Locate every blood parasite and identify its species.
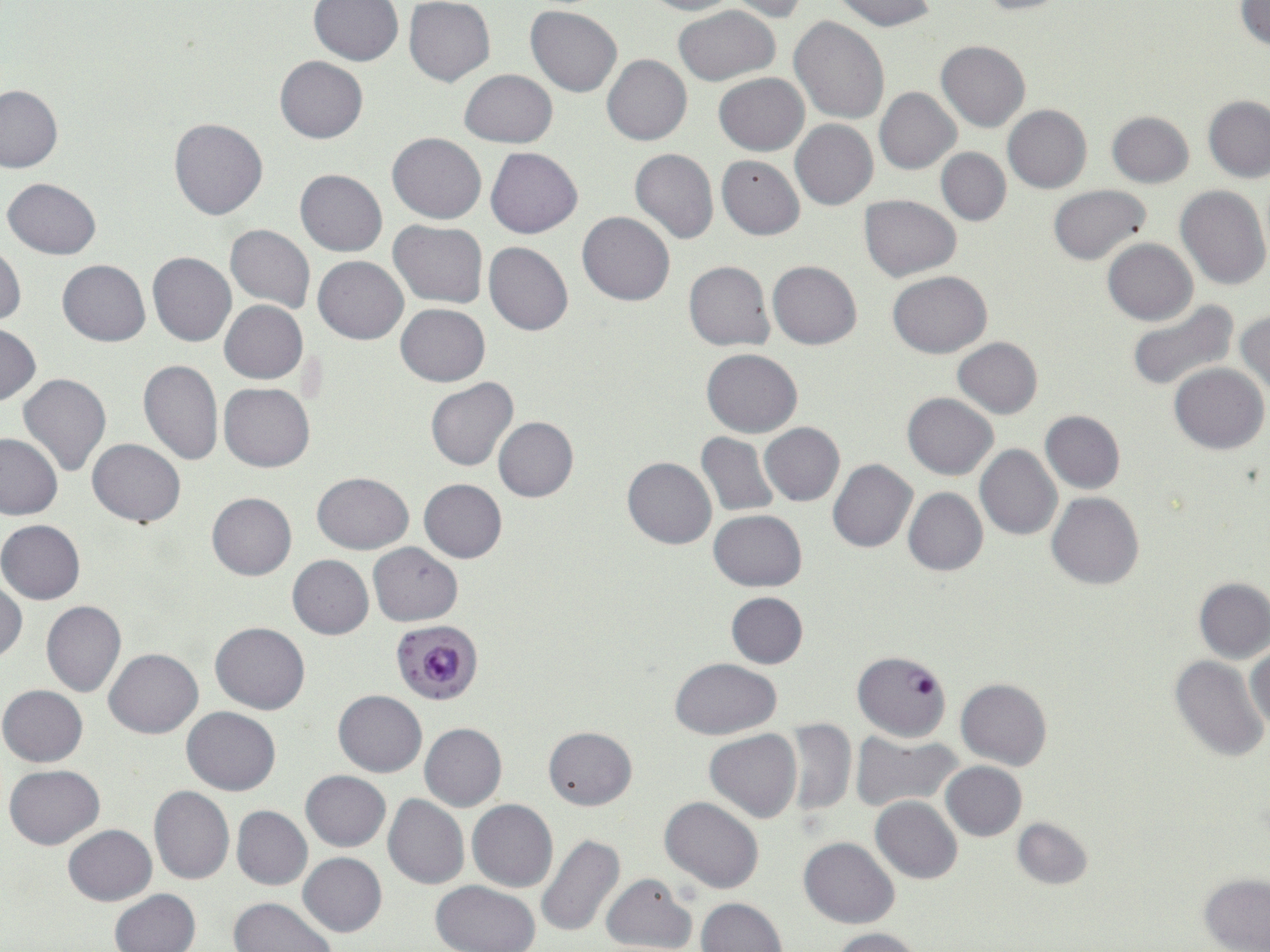

Approximate bounding boxes as named x1/y1/x2/y2 corners in pixels.
Plasmodium falciparum-infected red blood cells: (x1=390, y1=620, x2=482, y2=705), (x1=852, y1=650, x2=952, y2=741).
No Plasmodium ovale, Plasmodium malariae, Plasmodium vivax, Babesia divergens, or Trypanosoma brucei observed.

Uninfected red blood cell locations: (x1=640, y1=0, x2=741, y2=15), (x1=833, y1=0, x2=937, y2=30), (x1=969, y1=0, x2=1067, y2=15), (x1=310, y1=1, x2=403, y2=67), (x1=405, y1=1, x2=495, y2=86), (x1=724, y1=1, x2=809, y2=21), (x1=1235, y1=1, x2=1270, y2=51), (x1=673, y1=4, x2=780, y2=85), (x1=526, y1=6, x2=622, y2=97), (x1=788, y1=16, x2=889, y2=123), (x1=936, y1=41, x2=1030, y2=131), (x1=602, y1=54, x2=692, y2=145), (x1=274, y1=56, x2=367, y2=143), (x1=460, y1=68, x2=556, y2=148), (x1=714, y1=74, x2=809, y2=155), (x1=0, y1=85, x2=64, y2=173), (x1=875, y1=87, x2=961, y2=174), (x1=1203, y1=95, x2=1270, y2=182), (x1=1003, y1=105, x2=1092, y2=192), (x1=1106, y1=111, x2=1194, y2=187), (x1=169, y1=118, x2=267, y2=220), (x1=791, y1=120, x2=878, y2=210), (x1=388, y1=133, x2=487, y2=224), (x1=487, y1=147, x2=582, y2=238), (x1=630, y1=148, x2=718, y2=244), (x1=937, y1=148, x2=1011, y2=225), (x1=716, y1=154, x2=805, y2=240), (x1=295, y1=169, x2=387, y2=256), (x1=2, y1=178, x2=103, y2=258), (x1=1047, y1=184, x2=1152, y2=264), (x1=1175, y1=184, x2=1270, y2=291), (x1=859, y1=195, x2=960, y2=281), (x1=578, y1=212, x2=675, y2=306), (x1=390, y1=219, x2=488, y2=308), (x1=225, y1=224, x2=315, y2=313), (x1=1103, y1=239, x2=1197, y2=325), (x1=484, y1=242, x2=573, y2=337), (x1=0, y1=244, x2=26, y2=326), (x1=148, y1=252, x2=237, y2=346), (x1=313, y1=256, x2=408, y2=344), (x1=58, y1=260, x2=150, y2=345), (x1=768, y1=260, x2=861, y2=349), (x1=684, y1=261, x2=774, y2=351), (x1=887, y1=271, x2=993, y2=357), (x1=1127, y1=299, x2=1240, y2=392), (x1=220, y1=301, x2=308, y2=382), (x1=396, y1=303, x2=489, y2=386), (x1=1234, y1=311, x2=1270, y2=398), (x1=0, y1=324, x2=41, y2=406), (x1=951, y1=337, x2=1042, y2=419), (x1=701, y1=349, x2=802, y2=437), (x1=138, y1=359, x2=223, y2=466), (x1=1169, y1=363, x2=1268, y2=454), (x1=19, y1=373, x2=112, y2=478), (x1=426, y1=378, x2=518, y2=471), (x1=220, y1=383, x2=315, y2=471), (x1=902, y1=393, x2=998, y2=480), (x1=1040, y1=410, x2=1125, y2=493), (x1=494, y1=417, x2=577, y2=502), (x1=760, y1=423, x2=845, y2=505), (x1=696, y1=433, x2=778, y2=516), (x1=0, y1=434, x2=64, y2=520), (x1=87, y1=438, x2=185, y2=526), (x1=976, y1=445, x2=1062, y2=541), (x1=623, y1=457, x2=717, y2=549), (x1=828, y1=460, x2=917, y2=552), (x1=312, y1=472, x2=414, y2=553), (x1=419, y1=478, x2=507, y2=562), (x1=903, y1=488, x2=988, y2=575), (x1=1046, y1=491, x2=1144, y2=590), (x1=207, y1=492, x2=296, y2=580), (x1=709, y1=510, x2=808, y2=591), (x1=1, y1=519, x2=85, y2=604), (x1=369, y1=542, x2=462, y2=627), (x1=286, y1=555, x2=373, y2=639), (x1=1194, y1=579, x2=1270, y2=663), (x1=0, y1=580, x2=26, y2=664), (x1=726, y1=592, x2=807, y2=667), (x1=41, y1=600, x2=126, y2=697), (x1=212, y1=622, x2=309, y2=714), (x1=1247, y1=644, x2=1269, y2=733), (x1=104, y1=648, x2=203, y2=739), (x1=1169, y1=655, x2=1267, y2=763), (x1=670, y1=658, x2=781, y2=739), (x1=955, y1=679, x2=1053, y2=770), (x1=0, y1=686, x2=87, y2=767), (x1=334, y1=690, x2=426, y2=776), (x1=183, y1=707, x2=280, y2=795), (x1=784, y1=718, x2=856, y2=817), (x1=419, y1=723, x2=507, y2=811), (x1=544, y1=726, x2=637, y2=809), (x1=704, y1=729, x2=801, y2=822), (x1=853, y1=730, x2=959, y2=813), (x1=942, y1=761, x2=1027, y2=841), (x1=4, y1=764, x2=104, y2=849), (x1=301, y1=770, x2=390, y2=851), (x1=148, y1=786, x2=235, y2=884), (x1=383, y1=795, x2=469, y2=890), (x1=660, y1=796, x2=763, y2=894), (x1=871, y1=797, x2=962, y2=883), (x1=468, y1=800, x2=557, y2=892), (x1=232, y1=805, x2=313, y2=890), (x1=1012, y1=817, x2=1092, y2=889), (x1=63, y1=824, x2=156, y2=905), (x1=535, y1=834, x2=625, y2=936), (x1=798, y1=837, x2=899, y2=928), (x1=298, y1=852, x2=386, y2=936), (x1=600, y1=873, x2=696, y2=952), (x1=1200, y1=874, x2=1270, y2=951), (x1=430, y1=881, x2=541, y2=952), (x1=108, y1=889, x2=199, y2=952), (x1=228, y1=897, x2=336, y2=952), (x1=697, y1=897, x2=785, y2=951), (x1=827, y1=927, x2=927, y2=952). Slide-level diagnosis: Plasmodium falciparum. Optical microscopy. Image is 1270×952 pixels. One field of a larger specimen. May-Grünwald-Giemsa stain. Thin blood smear. 1000x magnification.